Identify the preparation type.
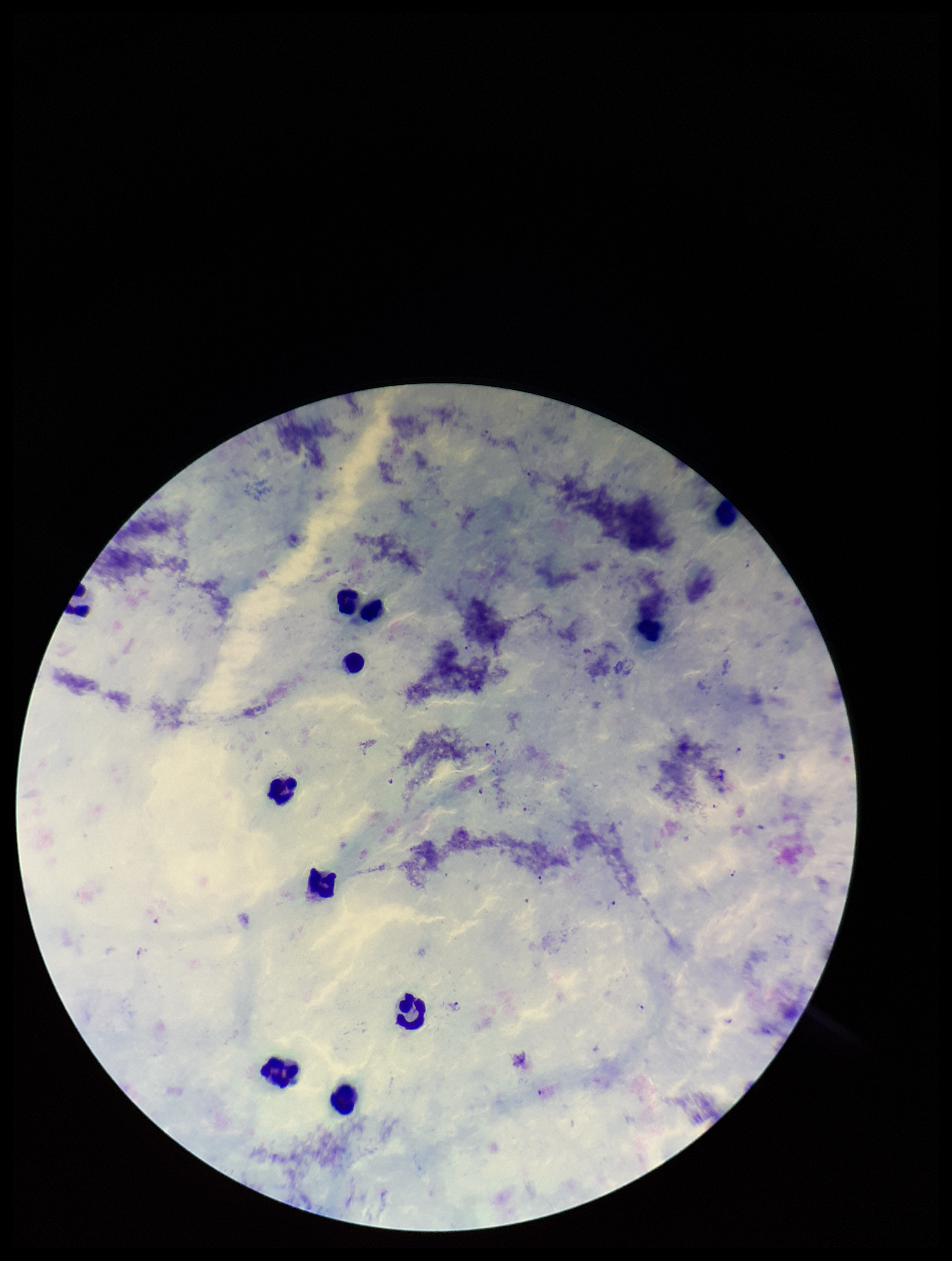

Thick.

Summary:
  - Parasite count: 9
  - Field of view: one from this slide
  - Stain: Giemsa
  - Patient malaria status: infected
  - Leukocyte count: 10
  - Image size: 952×1261 pixels
  - Capture: smartphone photograph through the microscope eyepiece
  - Species reported for this patient: Plasmodium falciparum
  - Plasmodium parasites: detected